Describe the morphology of the red blood cells.
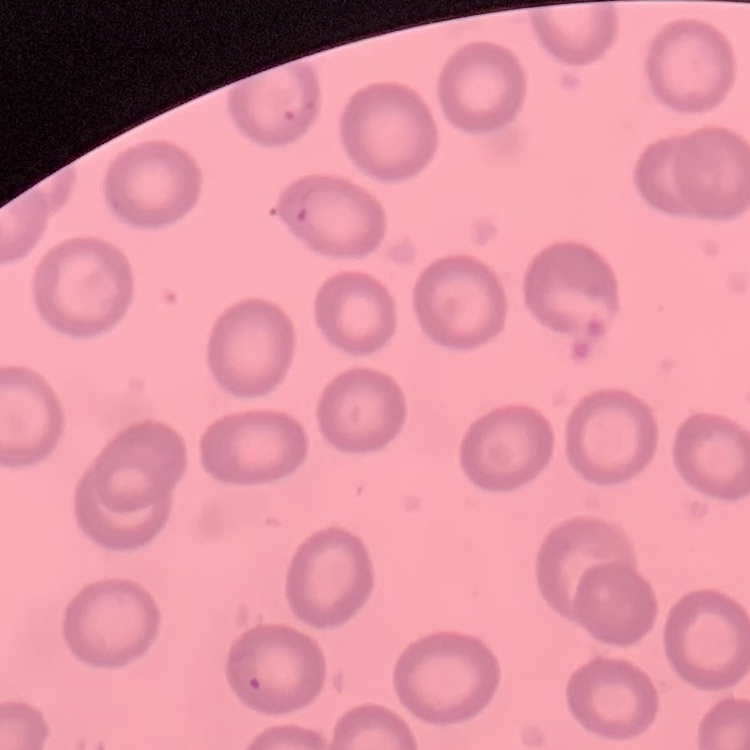

They show no rouleaux formation.

stain = Field's or Giemsa
image type = square crop of a larger photomicrograph
preparation = thin blood smear